Assess this cell for malaria.
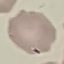

Uninfected.

Thin blood smear. Giemsa-stained preparation. Cell patch, automatically extracted from a larger field of view and resized to 64 × 64 pixels. Photographed with a smartphone camera at the microscope eyepiece.